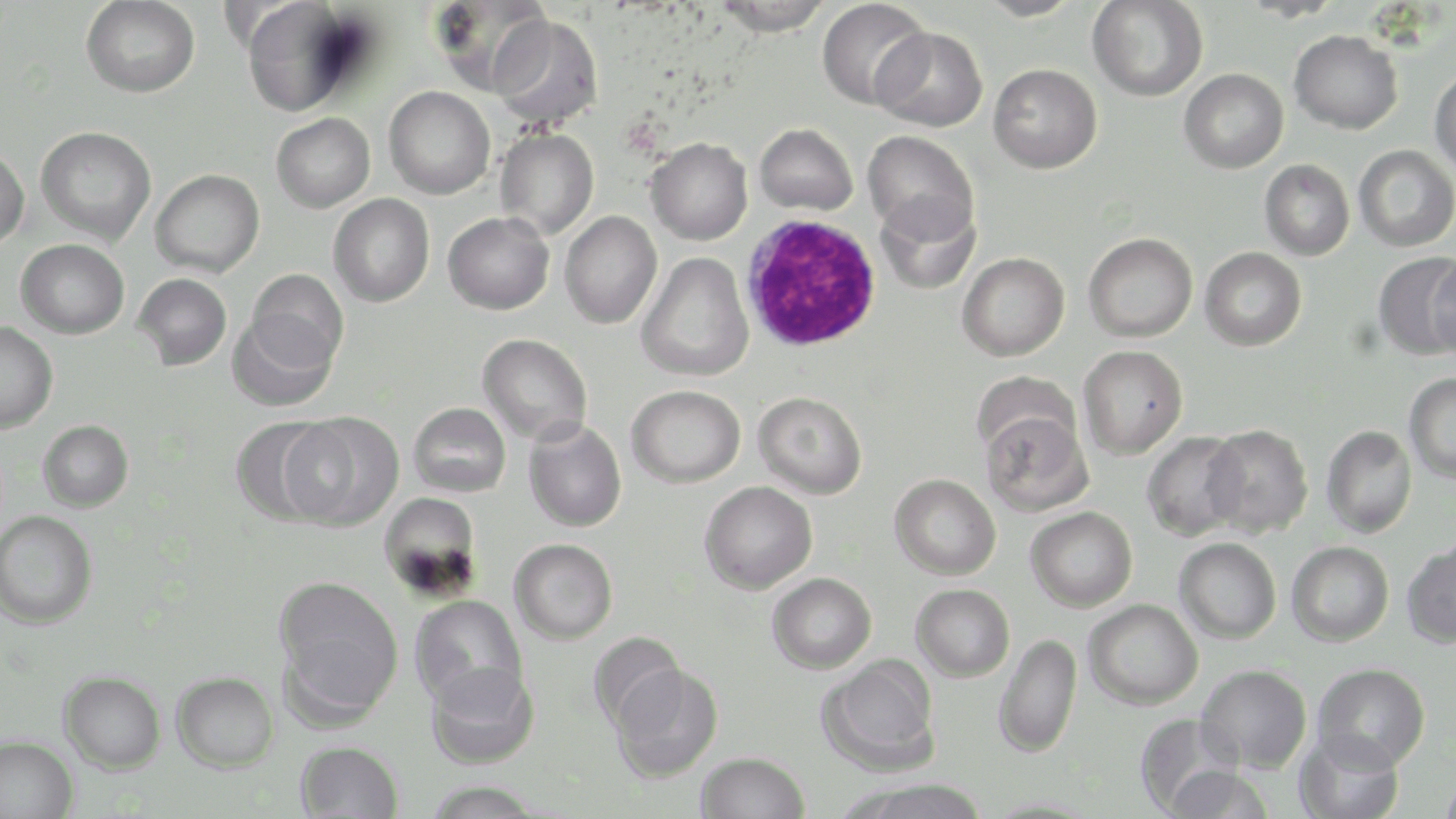

slide-level diagnosis = Plasmodium falciparum
preparation = thin blood smear
image size = 1456×819 pixels
uninfected red blood cell locations = approximate bounding boxes as (x1,y1)-(x2,y2) corner pairs in pixels: (81,0)-(200,98), (428,0)-(553,96), (711,0)-(833,36), (816,0)-(932,111), (975,0)-(1082,21), (240,1)-(363,118), (1087,1)-(1208,102), (490,14)-(604,130), (872,27)-(988,132), (1288,29)-(1403,135), (988,63)-(1103,174), (1430,64)-(1456,175), (1178,68)-(1289,174), (383,86)-(496,200), (271,113)-(375,213), (755,123)-(858,215), (36,126)-(157,245), (495,127)-(599,240), (863,130)-(979,242), (646,137)-(753,245), (0,143)-(29,249), (1353,145)-(1456,252), (1259,159)-(1355,260), (151,168)-(265,277), (875,193)-(981,294), (328,194)-(435,307), (559,211)-(662,329), (443,212)-(555,315), (1083,232)-(1198,342), (16,238)-(130,338), (1199,246)-(1307,351), (635,252)-(754,382), (957,252)-(1070,362), (1373,253)-(1456,360), (1427,254)-(1456,360), (246,268)-(349,372), (133,273)-(232,370), (227,313)-(338,412), (0,321)-(58,433), (477,333)-(593,445), (1077,345)-(1188,460), (971,370)-(1081,461), (1404,373)-(1456,483), (626,385)-(746,488), (753,391)-(867,499), (408,402)-(511,498), (980,409)-(1093,517), (281,411)-(404,532), (230,416)-(339,526), (523,418)-(627,532), (38,420)-(134,512), (1202,424)-(1314,538), (1321,425)-(1417,538), (1141,431)-(1248,541), (889,474)-(1001,580), (699,481)-(817,594), (378,491)-(483,599), (1025,506)-(1137,612), (0,509)-(98,629), (1174,537)-(1282,644), (509,538)-(618,644), (1402,540)-(1456,649), (1287,541)-(1394,647), (767,572)-(877,674), (273,574)-(403,720), (910,584)-(1015,682), (410,595)-(527,710), (1083,599)-(1203,710), (587,632)-(685,733), (992,633)-(1083,759), (818,655)-(942,775), (425,661)-(540,770), (1312,662)-(1431,771), (610,663)-(723,783), (1196,664)-(1312,773), (59,670)-(165,773), (171,671)-(279,772), (1135,713)-(1242,815), (1294,731)-(1405,819), (0,735)-(78,819), (295,740)-(404,819), (695,752)-(810,818), (1164,764)-(1274,819), (1438,770)-(1456,819), (425,779)-(544,819), (836,779)-(991,819), (977,796)-(1105,818)
white blood cell locations = approximate bounding boxes as (x1,y1)-(x2,y2) corner pairs in pixels: (741,214)-(882,353)
modality = light microscopy
stain = May-Grünwald-Giemsa
magnification = 1000x
field of view = single